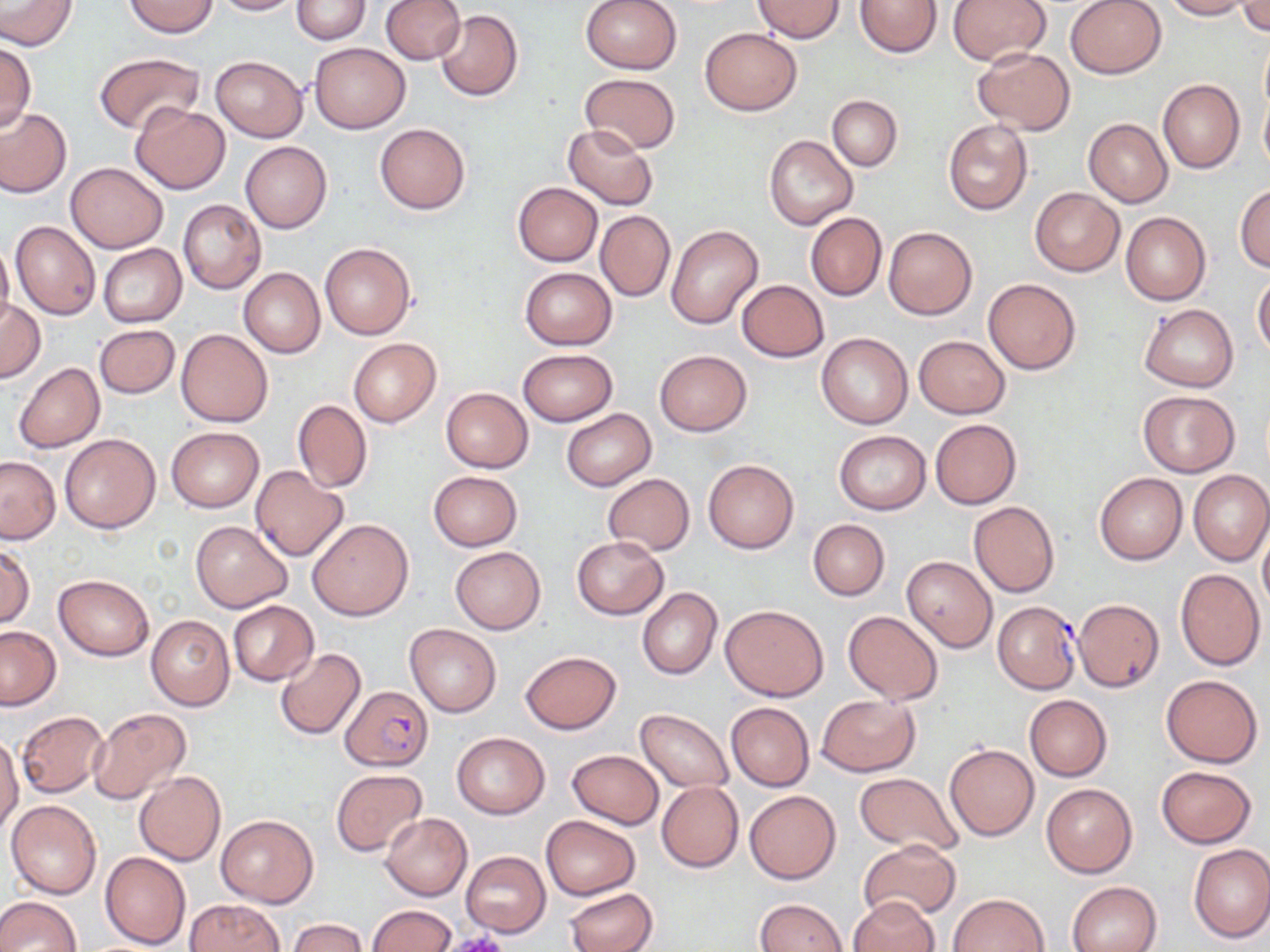

Summary:
  - Coordinate format: approximate bounding boxes as (x1,y1)-(x2,y2) corner pairs in pixels
  - Uninfected red blood cell locations: (0,0)-(76,50), (211,0)-(302,15), (292,0)-(370,44), (380,0)-(465,64), (579,0)-(682,74), (855,0)-(942,57), (948,0)-(1051,66), (1065,0)-(1167,79), (1160,0)-(1252,20), (123,1)-(219,37), (753,1)-(845,41), (1238,2)-(1270,36), (434,10)-(524,102), (700,28)-(802,115), (0,41)-(36,131), (308,42)-(409,133), (972,48)-(1075,134), (94,53)-(204,133), (210,56)-(307,142), (580,73)-(681,154), (1157,79)-(1245,173), (1260,86)-(1270,175), (828,94)-(902,171), (130,103)-(230,193), (0,108)-(71,197), (1084,118)-(1172,207), (943,119)-(1033,216), (375,123)-(470,214), (562,123)-(660,210), (765,135)-(858,231), (241,142)-(332,232), (65,162)-(168,253), (512,182)-(602,265), (1234,183)-(1270,273), (1029,187)-(1124,276), (178,199)-(266,294), (1120,210)-(1210,306), (596,211)-(674,301), (805,212)-(886,301), (10,220)-(100,321), (666,225)-(763,329), (883,227)-(977,319), (0,241)-(15,334), (320,242)-(416,340), (98,244)-(187,326), (518,267)-(617,349), (239,268)-(325,358), (1253,273)-(1270,359), (983,277)-(1082,375), (736,280)-(829,361), (0,298)-(45,382), (1139,304)-(1239,391), (94,324)-(180,399), (177,329)-(273,426), (815,333)-(913,429), (914,335)-(1009,418), (349,338)-(441,426), (517,348)-(619,426), (655,349)-(751,436), (13,363)-(104,453), (440,387)-(533,473), (1138,390)-(1238,477), (293,399)-(372,492), (561,408)-(655,491), (930,419)-(1020,508), (166,426)-(264,512), (834,430)-(931,515), (59,433)-(161,533), (0,455)-(61,543), (703,460)-(799,553), (249,465)-(347,560), (1188,469)-(1270,566), (429,471)-(523,550), (1095,472)-(1187,565), (602,473)-(694,556), (969,502)-(1059,598), (308,519)-(413,620), (808,519)-(889,601), (192,520)-(292,612), (1259,522)-(1270,618), (572,536)-(670,619), (0,545)-(33,628), (451,546)-(545,634), (901,557)-(998,652), (1175,568)-(1266,670), (53,574)-(154,660), (637,588)-(721,679), (1073,598)-(1164,692), (229,601)-(318,685), (721,604)-(828,701), (843,610)-(943,704), (146,615)-(235,710), (404,623)-(501,717), (1,626)-(61,712), (274,648)-(366,739), (520,651)-(621,735), (1161,674)-(1263,767), (817,694)-(920,776), (1024,694)-(1111,780), (725,702)-(813,791), (87,708)-(189,805), (635,709)-(734,793), (16,711)-(109,798), (451,732)-(550,818), (0,733)-(23,838), (944,744)-(1039,841), (567,750)-(663,829), (1157,765)-(1255,847), (331,768)-(426,856), (855,769)-(964,857), (134,772)-(225,866), (656,782)-(743,873), (1040,782)-(1137,878), (744,790)-(840,884), (6,800)-(102,899), (216,813)-(318,908), (381,814)-(472,899), (541,815)-(639,899), (859,838)-(962,921), (1188,844)-(1270,943), (461,850)-(550,937), (101,851)-(191,950), (1068,881)-(1161,952), (565,887)-(658,952), (950,892)-(1049,952), (0,896)-(80,951), (848,896)-(938,952), (754,897)-(847,951), (183,899)-(282,952), (366,904)-(456,952), (287,918)-(367,952)
  - Plasmodium falciparum-infected red blood cell locations: (994,600)-(1080,692), (341,686)-(434,771)
  - Platelet locations: (440,933)-(510,952)
  - Slide-level diagnosis: Plasmodium falciparum
  - Field of view: single
  - Magnification: 1000x
  - Image size: 1270×952 pixels
  - Modality: light microscopy
  - Preparation: thin blood film
  - Stain: May-Grünwald-Giemsa